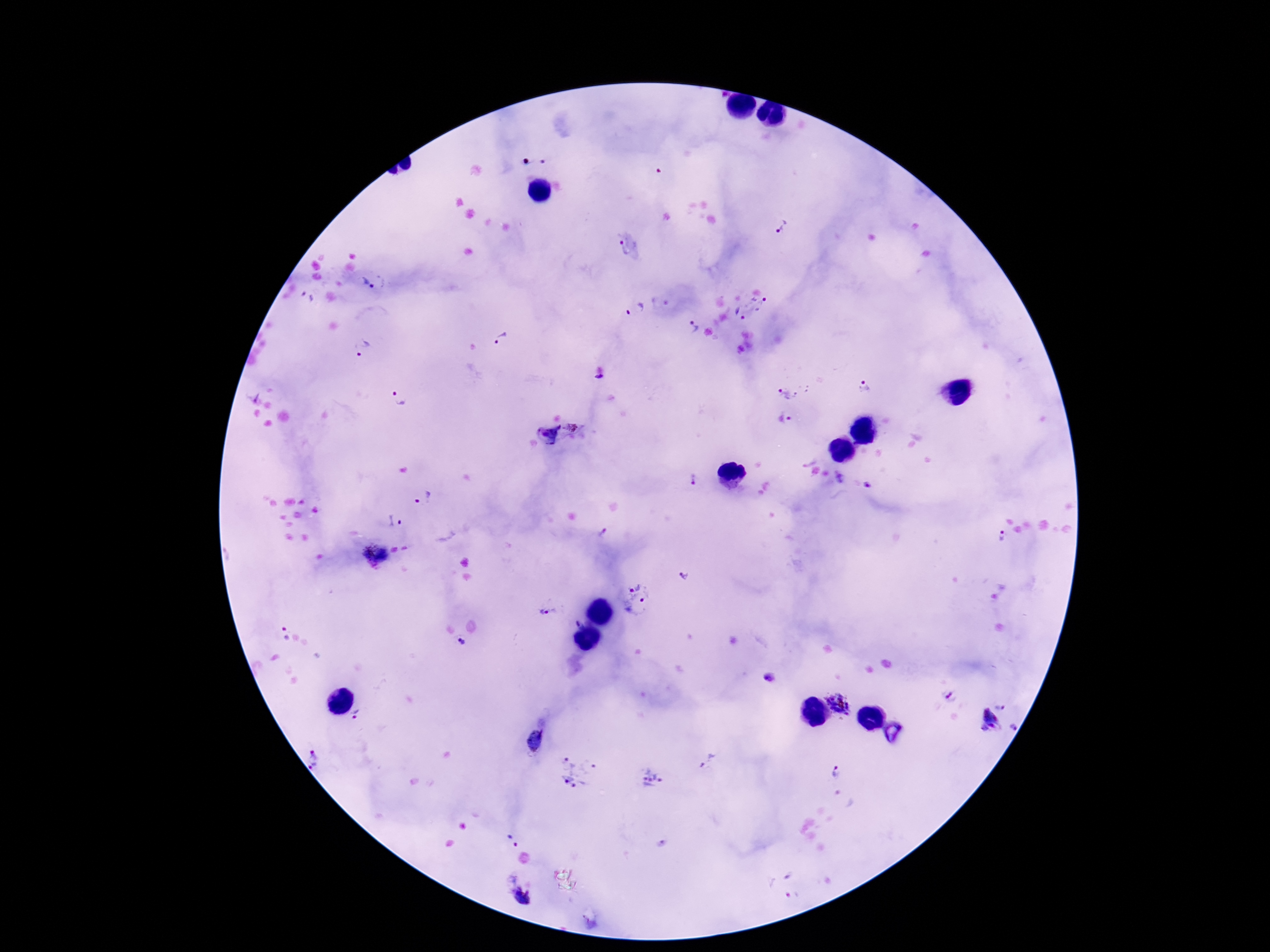 Approximate centers as {x, y} in pixels. Plasmodium parasite locations: {781, 229}, {627, 249}, {368, 284}, {307, 297}, {760, 304}, {636, 310}, {740, 313}, {693, 327}, {501, 339}, {360, 348}, {600, 377}, {866, 388}, {789, 391}, {399, 396}, {254, 398}, {790, 418}, {573, 427}, {547, 434}, {692, 479}, {840, 479}, {869, 485}, {423, 498}, {395, 522}, {604, 534}, {1002, 536}, {375, 555}, {684, 576}, {637, 600}, {549, 610}, {577, 622}, {283, 635}, {462, 642}, {771, 678}, {951, 697}, {837, 703}, {1001, 706}, {358, 713}, {987, 723}, {1012, 728}, {316, 758}, {707, 763}, {834, 770}, {577, 771}, {651, 778}, {512, 842}, {791, 874}, {793, 893}, {524, 897}. Photographed through the microscope eyepiece with a smartphone camera. One field from this slide. Giemsa-stained preparation. Patient malaria status: positive. Image is 1270×952 pixels. 100x magnification. Thick blood smear.